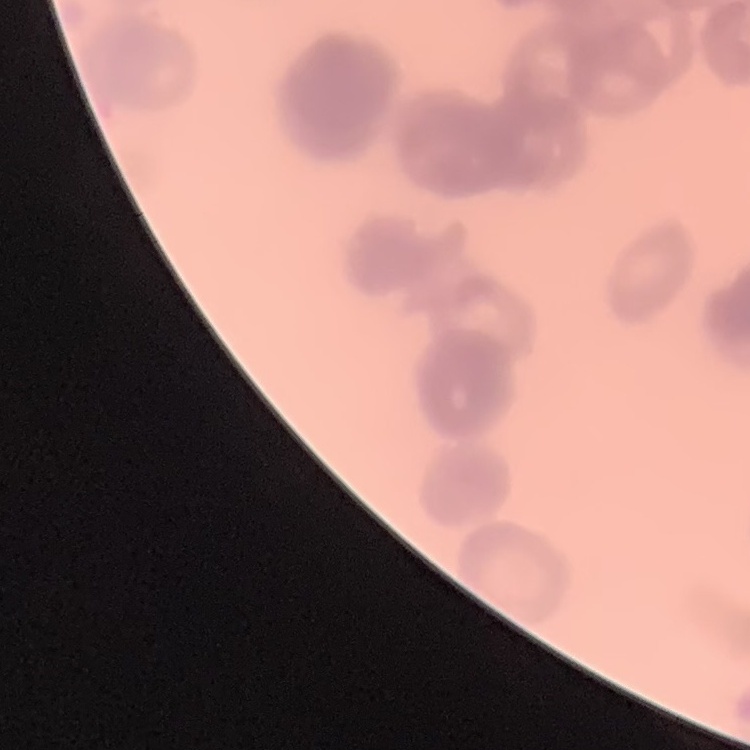

Summary:
  - Red blood cell morphology: rouleaux formation
  - Preparation: thin blood smear
  - Image type: square crop of a larger photomicrograph
  - Stain: Field's or Giemsa